Name the parasite shown.
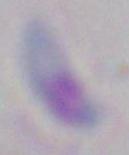

Toxoplasma gondii.

{
  "modality": "photomicrograph",
  "magnification": "1000x"
}